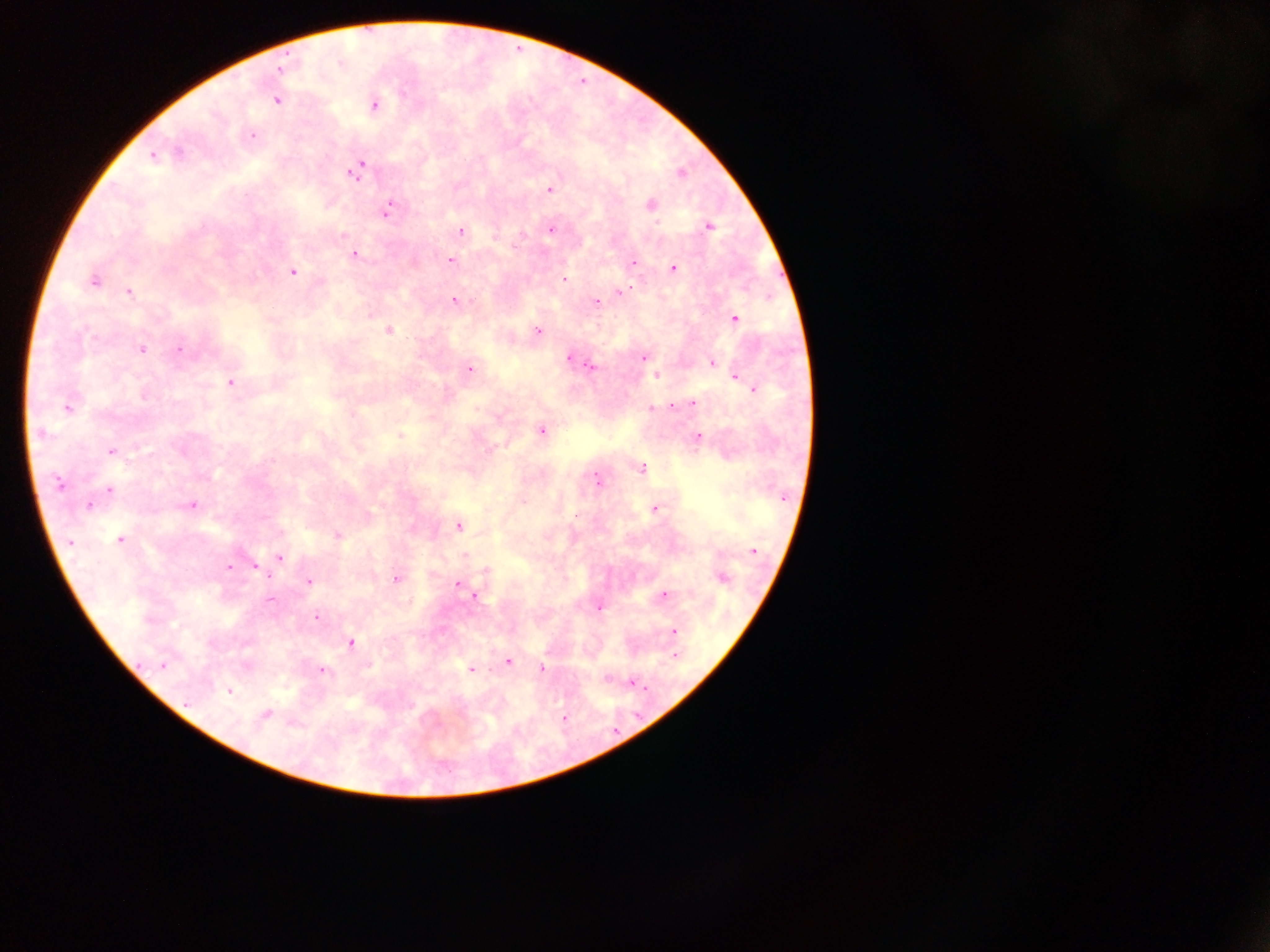
Approximate centers as (x, y) in pixels.
Summary:
  - Malaria parasite locations: (281, 69), (276, 100), (374, 105), (253, 135), (178, 152), (153, 157), (360, 165), (353, 172), (680, 172), (550, 190), (650, 204), (389, 209), (656, 222), (709, 226), (551, 229), (461, 231), (353, 254), (451, 261), (634, 262), (674, 268), (293, 272), (564, 279), (93, 281), (621, 291), (129, 292), (454, 300), (596, 302), (735, 319), (388, 331), (538, 331), (142, 350), (180, 350), (644, 357), (569, 358), (712, 363), (590, 366), (470, 370), (656, 375), (737, 379), (745, 382), (230, 383), (752, 387), (144, 396), (693, 404), (673, 406), (68, 407), (651, 409), (541, 430), (41, 434), (400, 435), (698, 437), (111, 451), (491, 451), (642, 469), (597, 480), (58, 483), (109, 490), (524, 501), (192, 505), (89, 506), (655, 508), (458, 526), (338, 535), (120, 540), (70, 542), (754, 551), (466, 555), (279, 557), (229, 567), (258, 569), (487, 571), (721, 578), (395, 579), (309, 581), (458, 584), (664, 594), (474, 596), (270, 599), (599, 607), (316, 617), (674, 631), (351, 643), (674, 656), (508, 661), (163, 665), (541, 668), (470, 669), (322, 671), (633, 683), (229, 691), (188, 702), (266, 714), (563, 717)
  - Field of view: single
  - Image size: 1270×952 pixels
  - Preparation: thick blood film
  - Capture: mobile-phone photograph through a microscope
  - Country: Ghana